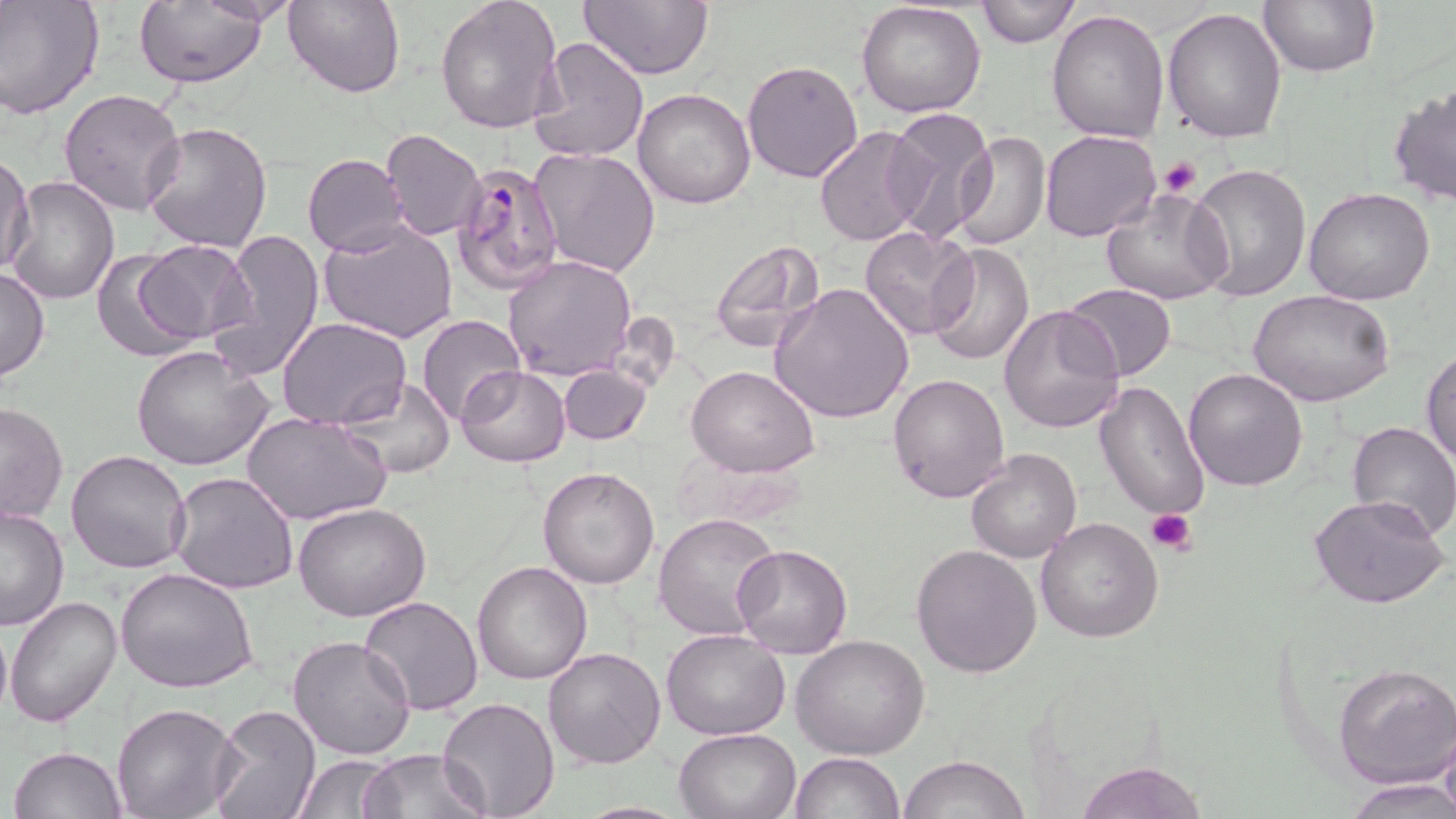

{
  "slide_level_diagnosis": "Plasmodium falciparum",
  "field_of_view": "single",
  "modality": "light microscopy",
  "plasmodium_falciparum_infected_red_blood_cell_locations": "approximate bounding boxes as (x1, y1, x2, y2) in pixels: (449, 158, 564, 295)",
  "magnification": "1000x",
  "uninfected_red_blood_cell_locations": "approximate bounding boxes as (x1, y1, x2, y2) in pixels: (0, 0, 104, 120), (284, 0, 405, 97), (435, 0, 565, 137), (581, 0, 713, 81), (975, 0, 1080, 48), (1258, 0, 1379, 78), (192, 1, 307, 25), (857, 1, 986, 117), (134, 2, 268, 87), (1163, 6, 1288, 144), (1046, 7, 1171, 144), (528, 34, 651, 163), (741, 59, 865, 183), (1388, 82, 1456, 206), (58, 87, 187, 217), (632, 88, 757, 209), (882, 109, 998, 246), (142, 120, 274, 254), (813, 126, 928, 247), (379, 128, 485, 242), (952, 130, 1051, 250), (1040, 130, 1161, 241), (530, 148, 661, 280), (0, 151, 33, 275), (302, 153, 409, 257), (1187, 163, 1314, 303), (5, 176, 122, 304), (1303, 186, 1435, 305), (1101, 189, 1231, 305), (320, 222, 458, 343), (860, 227, 978, 343), (214, 229, 324, 379), (136, 240, 256, 346), (708, 240, 827, 354), (924, 241, 1033, 366), (90, 249, 202, 363), (503, 253, 638, 381), (0, 268, 50, 379), (771, 281, 915, 423), (1065, 283, 1177, 382), (1250, 291, 1393, 406), (999, 305, 1126, 435), (416, 314, 525, 425), (278, 318, 411, 429), (131, 345, 274, 471), (1422, 348, 1456, 467), (456, 365, 570, 467), (560, 365, 651, 445), (686, 365, 820, 478), (1183, 368, 1308, 492), (888, 372, 1011, 504), (339, 378, 456, 479), (1094, 380, 1209, 521), (0, 401, 69, 525), (244, 412, 390, 527), (1347, 420, 1456, 539), (966, 447, 1083, 564), (67, 449, 193, 573), (538, 466, 659, 589), (169, 471, 298, 594), (1308, 494, 1451, 610), (294, 502, 432, 622), (1, 505, 70, 632), (654, 513, 782, 641), (1035, 517, 1163, 642), (912, 543, 1043, 679), (732, 544, 853, 659), (472, 560, 594, 684), (115, 568, 259, 695), (5, 594, 123, 727), (359, 595, 487, 716), (1, 617, 11, 728), (660, 627, 791, 741), (288, 635, 416, 759), (791, 635, 932, 758), (543, 646, 667, 768), (1333, 661, 1456, 788), (437, 697, 561, 817), (110, 702, 241, 819), (207, 702, 322, 819), (1437, 723, 1456, 819), (675, 726, 802, 818), (10, 746, 126, 819), (362, 748, 488, 818), (790, 750, 906, 819), (294, 754, 399, 818), (901, 754, 1028, 818), (1075, 759, 1208, 819), (1345, 778, 1456, 818), (571, 801, 695, 819)",
  "image_size": "1456×819 pixels",
  "preparation": "thin blood film",
  "platelet_locations": "approximate bounding boxes as (x1, y1, x2, y2) in pixels: (1158, 155, 1202, 197), (1147, 507, 1199, 553)",
  "stain": "May-Grünwald-Giemsa"
}